Describe the morphology of the red blood cells.
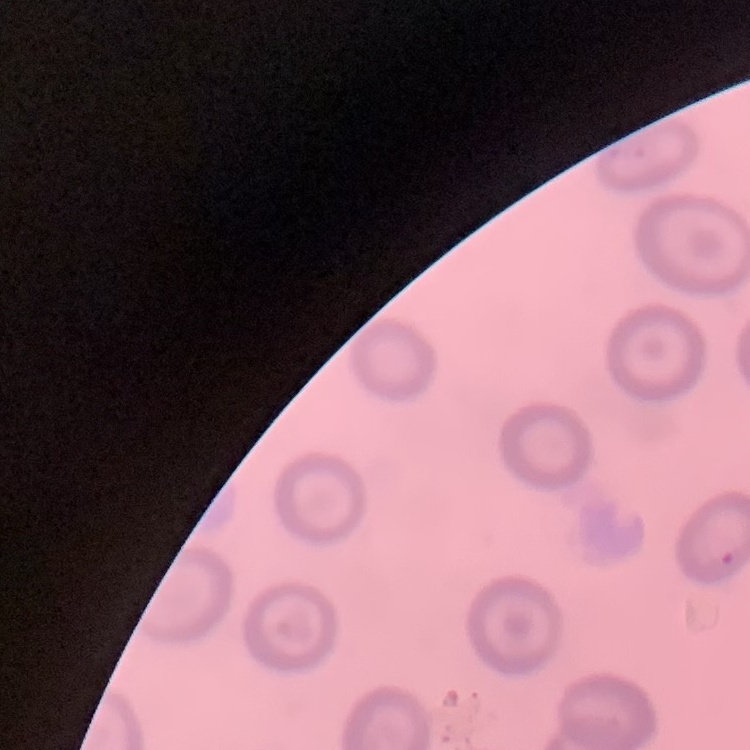
No rouleaux formation.

Square crop of a larger photomicrograph. Stained with either Field's or Giemsa. Thin blood film.